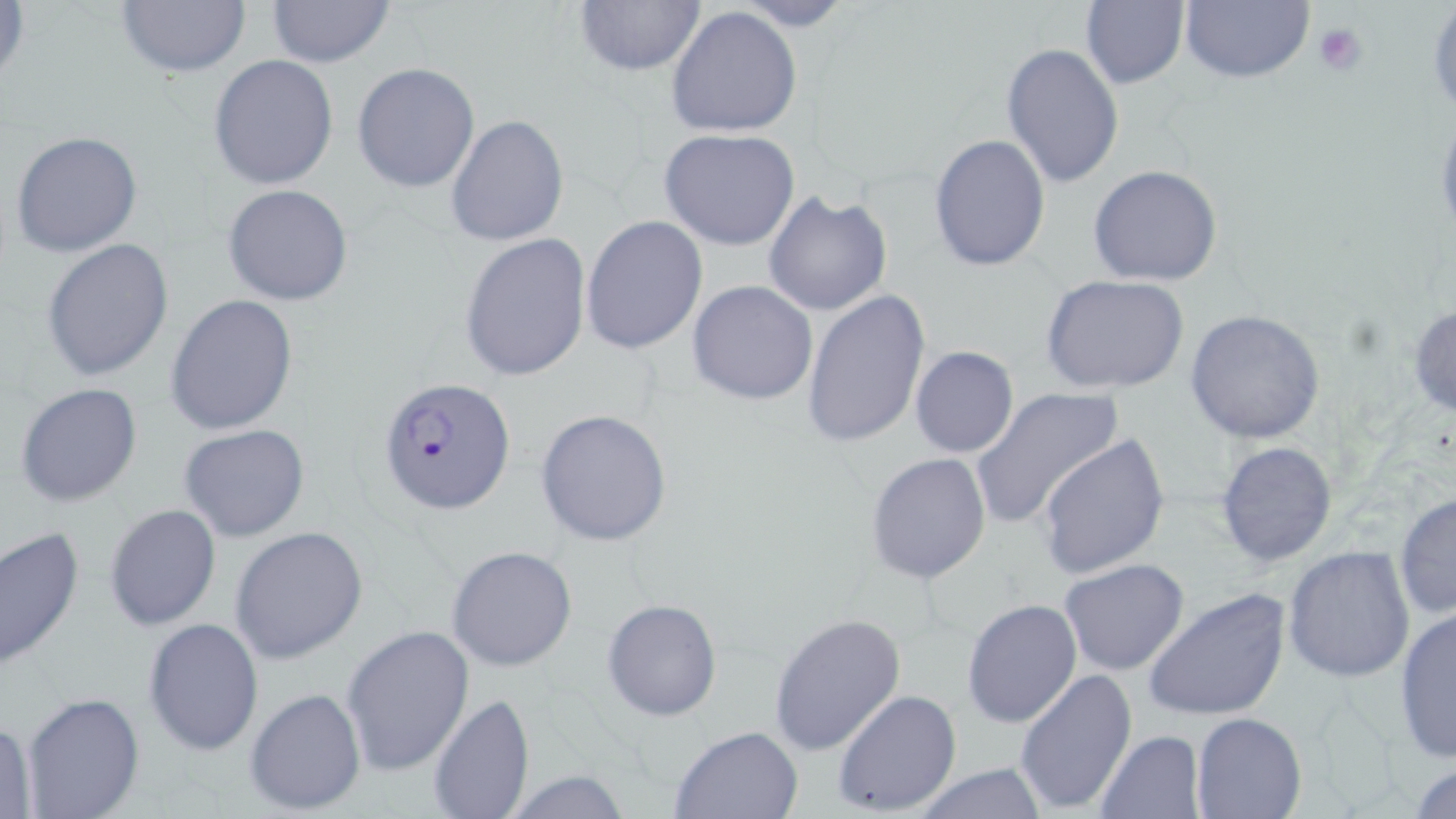
Summary:
  - Coordinate format: approximate bounding boxes as (x1, y1, x2, y2) in pixels
  - Plasmodium falciparum-infected red blood cell locations: (379, 377, 516, 512)
  - Platelet locations: (1314, 22, 1369, 76)
  - Uninfected red blood cell locations: (116, 0, 251, 76), (267, 0, 394, 68), (731, 0, 857, 31), (1179, 0, 1316, 84), (1427, 0, 1456, 118), (1, 1, 30, 93), (573, 1, 707, 78), (1081, 1, 1188, 89), (665, 6, 804, 138), (1001, 41, 1125, 187), (209, 54, 338, 189), (352, 62, 479, 193), (445, 113, 567, 248), (659, 127, 801, 250), (10, 129, 143, 257), (929, 134, 1051, 271), (1088, 165, 1222, 286), (222, 184, 352, 306), (762, 192, 894, 317), (582, 217, 708, 355), (459, 233, 591, 382), (42, 238, 173, 381), (1040, 274, 1190, 395), (688, 280, 819, 405), (804, 291, 929, 447), (167, 293, 297, 435), (1407, 303, 1456, 418), (1185, 309, 1325, 444), (909, 347, 1019, 458), (13, 382, 143, 507), (971, 387, 1123, 529), (535, 408, 673, 546), (179, 424, 310, 542), (1037, 434, 1170, 580), (1213, 440, 1339, 568), (865, 453, 992, 583), (1393, 491, 1456, 621), (103, 503, 222, 632), (0, 526, 86, 670), (230, 527, 369, 663), (446, 545, 578, 671), (1283, 547, 1416, 683), (1059, 559, 1190, 677), (1144, 587, 1291, 722), (960, 598, 1082, 728), (602, 599, 723, 720), (1392, 607, 1455, 764), (767, 611, 906, 758), (143, 618, 265, 758), (341, 624, 475, 776), (1014, 667, 1138, 814), (245, 687, 367, 815), (832, 689, 962, 814), (20, 690, 145, 819), (428, 691, 532, 817), (1191, 711, 1306, 818), (0, 718, 36, 819), (669, 724, 806, 818), (1095, 729, 1204, 817), (1409, 760, 1456, 816), (910, 763, 1049, 818), (497, 770, 635, 818)
  - Slide-level diagnosis: Plasmodium falciparum
  - Stain: May-Grünwald-Giemsa
  - Modality: light microscopy
  - Preparation: thin blood film
  - Magnification: 1000x
  - Field of view: single
  - Image size: 1456×819 pixels